Describe the morphology of the red blood cells.
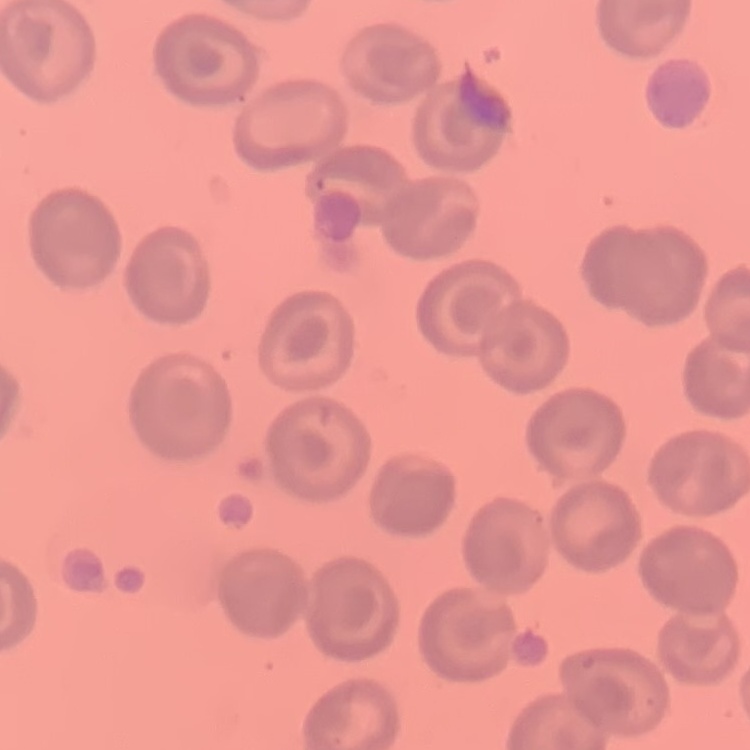
No rouleaux formation.

preparation = thin blood film
stain = Field's or Giemsa
image type = one tile cut from a larger photomicrograph